State the blood parasite species.
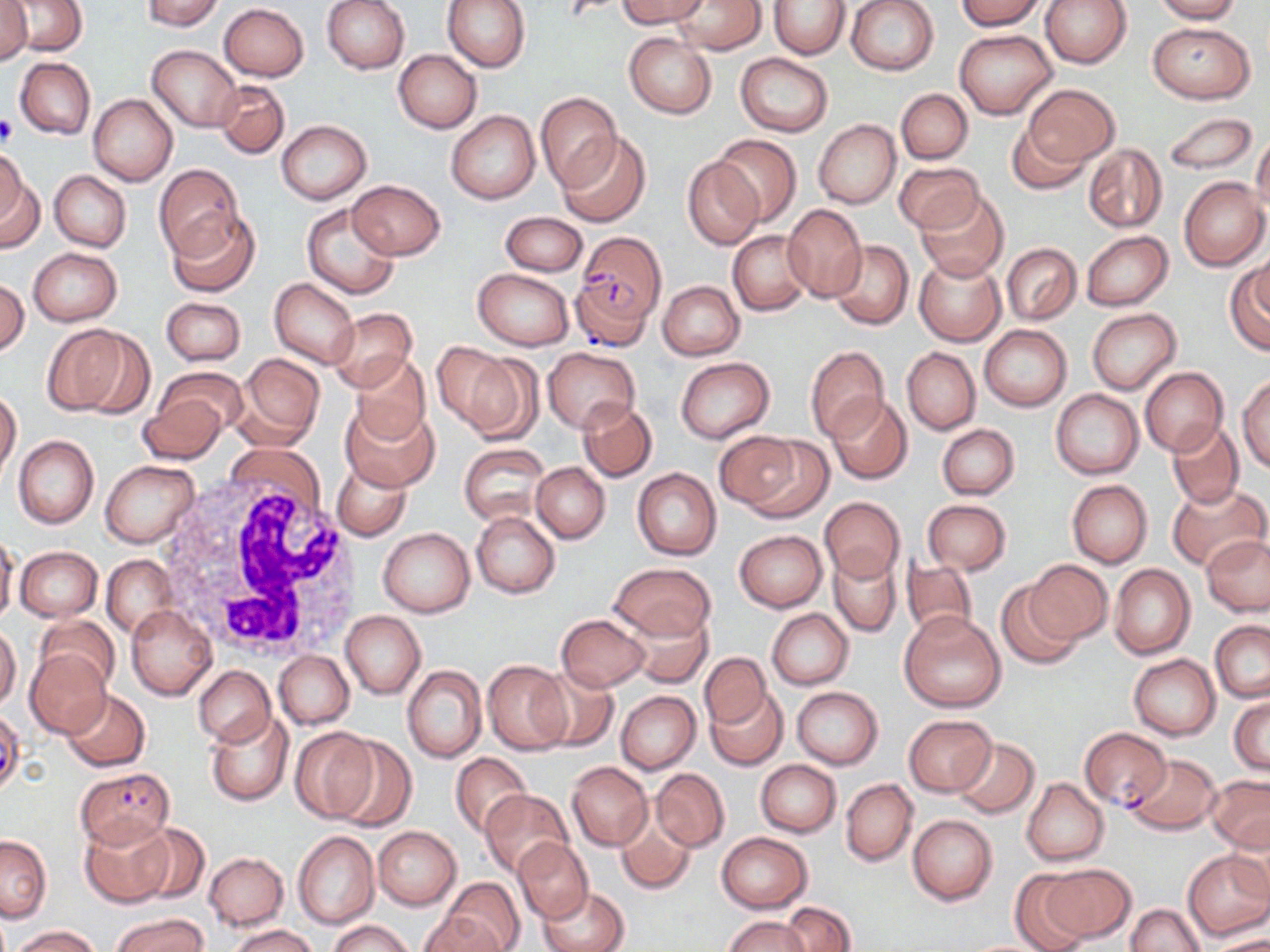

Plasmodium falciparum.

Summary:
  - Coordinate format: approximate bounding boxes as (x1,y1)-(x2,y2) corner pairs in pixels
  - White blood cell locations: (158,470)-(363,663)
  - Platelet locations: (0,114)-(17,148)
  - Uninfected red blood cell locations: (3,0)-(87,55), (141,0)-(225,30), (322,0)-(410,74), (442,0)-(530,73), (616,0)-(709,28), (672,0)-(767,54), (847,0)-(939,76), (957,0)-(1047,31), (1040,0)-(1131,69), (1152,0)-(1242,23), (769,1)-(850,58), (0,2)-(33,63), (219,3)-(309,81), (1147,22)-(1254,103), (954,29)-(1058,120), (623,31)-(717,119), (148,45)-(241,132), (393,49)-(482,133), (735,54)-(832,136), (15,57)-(95,140), (214,80)-(290,158), (1023,83)-(1120,168), (896,88)-(972,163), (534,91)-(621,192), (88,93)-(178,185), (446,110)-(540,204), (1162,110)-(1258,175), (1005,116)-(1091,195), (813,119)-(900,209), (277,120)-(371,204), (556,131)-(651,228), (1251,133)-(1270,221), (712,134)-(802,227), (1083,144)-(1167,233), (0,148)-(28,227), (682,157)-(763,250), (894,162)-(985,234), (153,163)-(244,259), (0,169)-(41,255), (49,170)-(131,252), (1180,176)-(1268,271), (347,179)-(445,260), (915,188)-(1009,281), (302,204)-(401,300), (782,204)-(868,302), (166,209)-(260,297), (499,212)-(588,277), (729,230)-(811,316), (1082,230)-(1173,310), (827,239)-(914,330), (1001,243)-(1081,324), (28,246)-(122,325), (1250,249)-(1270,321), (912,253)-(1006,346), (1225,264)-(1270,355), (473,269)-(573,350), (0,279)-(29,357), (269,279)-(359,368), (657,280)-(744,361), (161,297)-(246,366), (327,308)-(417,391), (1087,308)-(1181,395), (40,323)-(148,418), (979,325)-(1071,411), (435,344)-(533,436), (803,345)-(890,443), (543,347)-(639,434), (901,347)-(980,434), (235,353)-(325,447), (351,354)-(432,444), (675,357)-(776,443), (154,366)-(247,443), (1139,367)-(1227,455), (1238,375)-(1270,471), (1051,389)-(1144,479), (0,390)-(22,478), (139,392)-(229,464), (827,395)-(912,485), (577,398)-(657,482), (341,400)-(438,491), (1166,419)-(1245,509), (937,424)-(1019,500), (716,432)-(811,515), (13,435)-(99,527), (460,443)-(550,524), (101,460)-(202,548), (333,462)-(411,541), (531,462)-(610,544), (632,468)-(722,560), (1067,480)-(1152,567), (1166,482)-(1267,571), (821,497)-(905,583), (922,499)-(1011,573), (470,510)-(560,599), (378,527)-(475,616), (735,530)-(827,611), (0,533)-(20,629), (1201,535)-(1270,615), (15,545)-(102,622), (828,551)-(902,638), (100,555)-(177,639), (901,558)-(978,642), (1026,560)-(1112,644), (1108,563)-(1196,660), (609,564)-(716,642), (996,581)-(1085,671), (565,590)-(701,683), (126,604)-(216,700), (622,608)-(714,688), (767,608)-(854,690), (899,610)-(1007,713), (341,611)-(425,699), (557,614)-(651,691), (35,615)-(119,693), (1209,621)-(1270,701), (0,626)-(21,710), (25,650)-(111,739), (273,651)-(353,729), (700,653)-(771,729), (1129,654)-(1220,740), (482,659)-(570,755), (403,665)-(487,763), (194,666)-(275,747), (532,666)-(619,752), (707,685)-(787,770), (791,687)-(883,768), (61,688)-(150,771), (615,690)-(700,775), (1229,695)-(1269,775), (206,711)-(292,806), (903,715)-(996,796), (291,726)-(380,822), (953,736)-(1040,819), (329,737)-(417,832), (450,751)-(533,839), (1124,754)-(1222,835), (756,759)-(841,838), (566,761)-(652,850), (651,768)-(730,852), (755,769)-(914,847), (627,775)-(720,888), (1206,775)-(1270,852), (1023,778)-(1109,866), (840,779)-(917,866), (480,789)-(574,879), (613,811)-(697,896), (907,814)-(997,904), (79,815)-(176,909), (130,822)-(211,904), (373,825)-(462,910), (293,831)-(380,929), (717,832)-(812,912), (1,834)-(52,922), (512,837)-(594,923), (1183,849)-(1270,941), (203,853)-(289,929), (1040,863)-(1136,944), (1010,870)-(1095,952), (442,876)-(525,952), (537,884)-(629,952), (781,902)-(857,952), (1126,903)-(1205,952), (421,910)-(503,952), (113,913)-(207,952), (724,915)-(811,952), (326,919)-(417,952), (229,925)-(319,952), (11,926)-(103,951), (1212,933)-(1270,952)
  - Plasmodium falciparum-infected red blood cell locations: (575,231)-(663,340), (570,277)-(656,353), (0,711)-(30,794), (1079,726)-(1171,810), (76,768)-(174,848)
  - Image size: 1270×952 pixels
  - Magnification: 1000x
  - Modality: optical microscopy
  - Stain: May-Grünwald-Giemsa
  - Preparation: thin blood film
  - Field of view: single